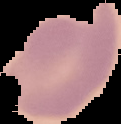
preparation = thin blood film
image size = 121×124 pixels
malaria status = uninfected
image type = cell region segmented out of the field of view; surrounding area masked to black